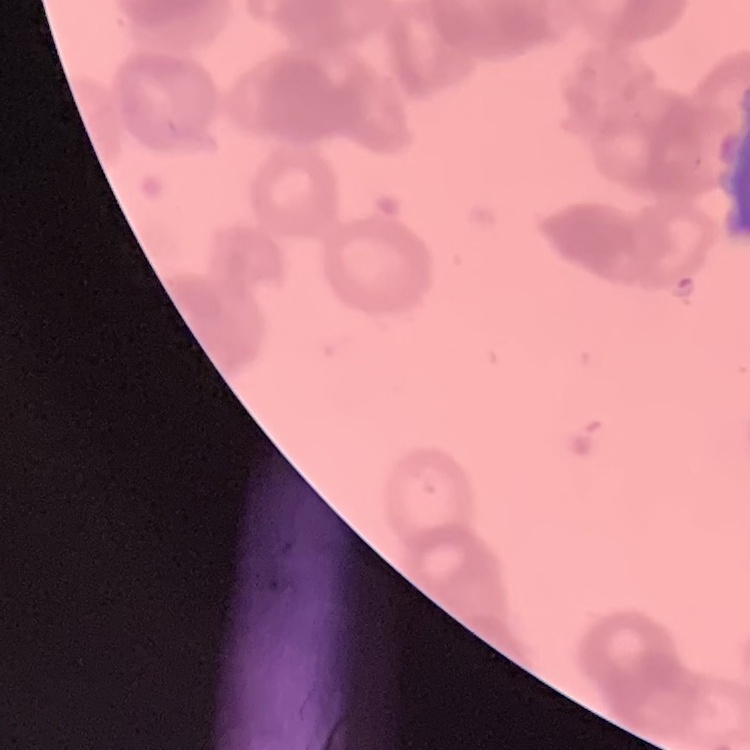
{
  "red_blood_cell_morphology": "rouleaux formation",
  "preparation": "thin blood smear",
  "image_type": "square crop of a larger photomicrograph",
  "stain": "Field's or Giemsa"
}